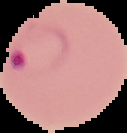

preparation = thin blood film
image size = 127×133 pixels
malaria status = parasitized
image type = cell region segmented out of the field of view; surrounding area masked to black